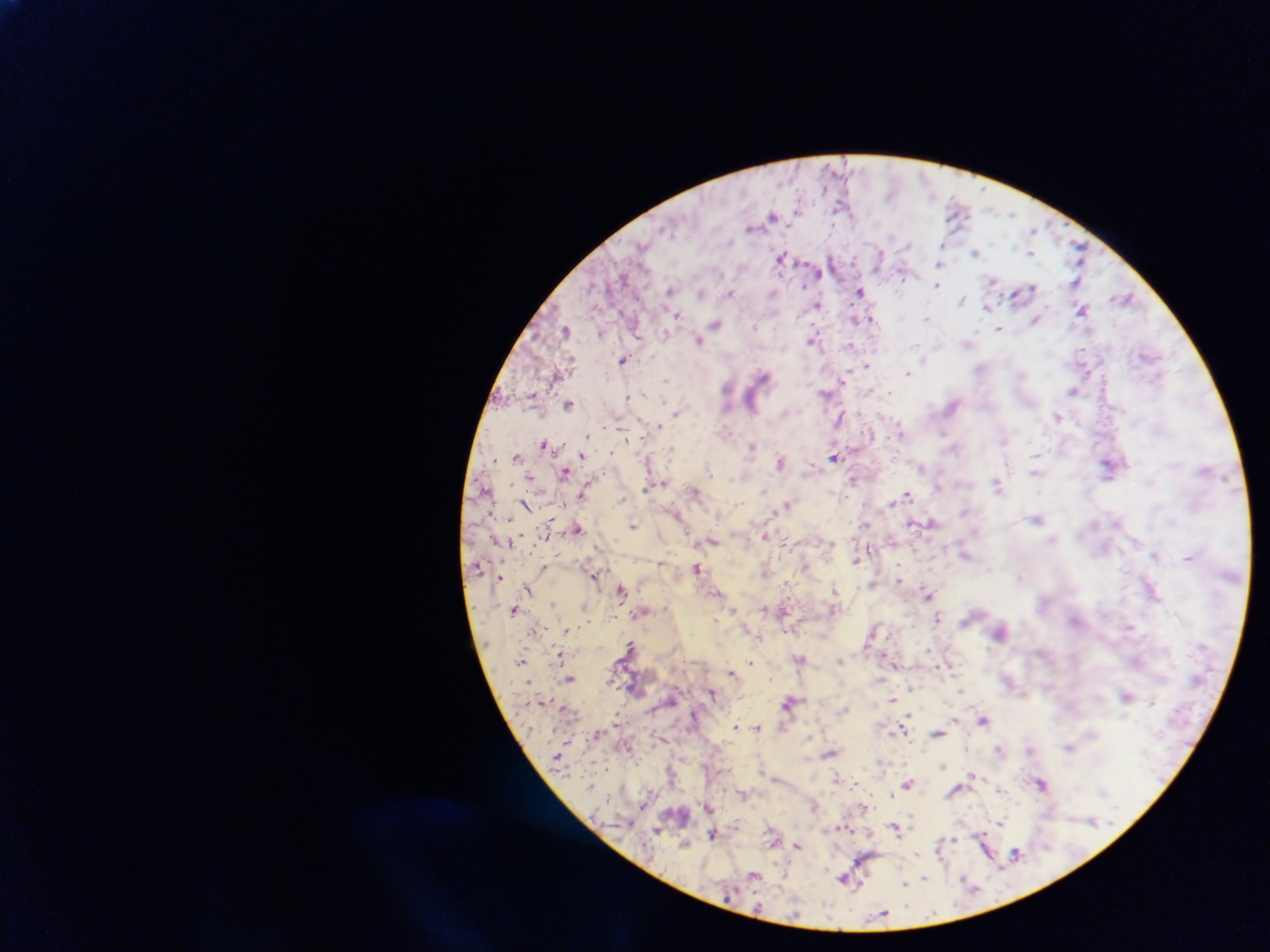
Plasmodium parasite locations = approximate centers as (x, y) in pixels: (799, 209), (957, 209), (772, 214), (1012, 215), (1033, 231), (891, 237), (908, 245), (940, 246), (975, 250), (1030, 252), (1078, 255), (781, 256), (939, 264), (819, 272), (902, 274), (993, 280), (1074, 282), (937, 285), (803, 288), (1033, 288), (861, 291), (702, 292), (732, 292), (1014, 294), (962, 298), (1125, 298), (986, 305), (818, 306), (1083, 309), (679, 315), (1035, 318), (856, 319), (871, 320), (924, 320), (717, 325), (755, 327), (565, 329), (998, 330), (699, 340), (812, 341), (967, 344), (851, 347), (1149, 351), (624, 359), (924, 360), (868, 367), (908, 373), (765, 377), (666, 380), (843, 380), (728, 390), (1072, 391), (642, 393), (825, 393), (629, 398), (568, 402), (678, 414), (838, 416), (1055, 417), (659, 425), (900, 430), (943, 433), (588, 437), (1004, 441), (543, 444), (672, 447), (751, 447), (613, 451), (582, 455), (1035, 455), (516, 457), (834, 457), (493, 459), (780, 463), (1105, 466), (1033, 471), (565, 472), (1036, 474), (853, 479), (663, 484), (997, 484), (644, 488), (765, 491), (695, 493), (583, 494), (908, 495), (788, 503), (892, 503), (509, 517), (1039, 519), (931, 523), (633, 524), (911, 525), (1116, 525), (867, 526), (578, 529), (766, 535), (1053, 537), (514, 540), (713, 541), (1153, 555), (856, 558), (661, 562), (542, 566), (697, 567), (592, 573), (500, 574), (1144, 578), (899, 581), (527, 589), (835, 589), (622, 590), (928, 595), (1157, 595), (553, 604), (583, 605), (767, 607), (733, 609), (513, 610), (833, 611), (938, 618), (715, 623), (1131, 626), (566, 630), (871, 635), (629, 643), (559, 653), (522, 659), (751, 660), (841, 660), (895, 664), (731, 672), (570, 678), (910, 684), (961, 690), (712, 692), (1128, 694), (892, 699), (543, 701), (788, 701), (843, 709), (615, 713), (980, 715), (734, 725), (758, 726), (901, 729), (904, 732), (939, 733), (595, 734), (830, 753), (942, 765), (603, 766), (972, 775), (836, 778), (909, 784), (1043, 785), (589, 786), (999, 789), (954, 793), (890, 795), (641, 805), (709, 807), (813, 807), (1000, 820), (1091, 820), (893, 828), (657, 831), (829, 832), (712, 835), (954, 841), (684, 845), (798, 845), (1016, 851), (753, 875), (926, 877), (844, 880), (906, 883), (907, 888), (883, 913)
capture = mobile-phone photograph through a microscope
field of view = single
preparation = thick blood smear
image size = 1270×952 pixels
country = Ghana